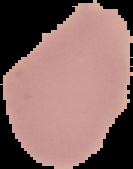
preparation = thin blood smear
image size = 133×169 pixels
malaria status = uninfected
image type = segmented cell region with the area outside set to black